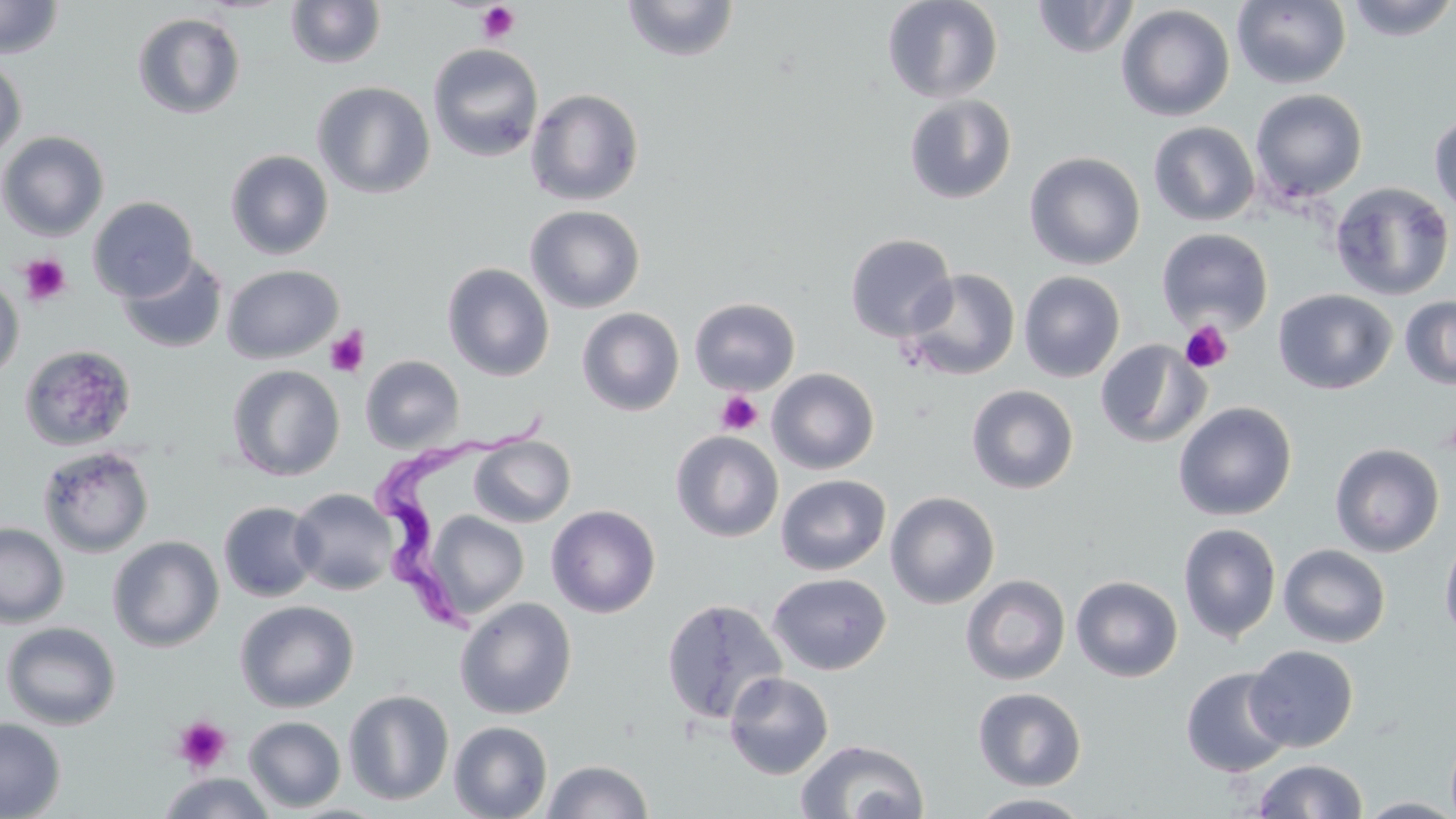 Approximate bounding boxes as (x1,y1)-(x2,y2) corner pairs in pixels. Trypanosoma brucei locations: (367,412)-(550,641). Uninfected red blood cell locations: (0,0)-(64,59), (620,0)-(740,62), (882,0)-(1003,103), (1031,0)-(1139,59), (1231,0)-(1352,89), (1343,0)-(1456,41), (285,1)-(387,69), (1116,4)-(1235,122), (131,12)-(246,120), (427,43)-(544,163), (0,57)-(27,161), (312,81)-(435,199), (526,88)-(645,206), (1249,89)-(1368,203), (904,95)-(1017,204), (1429,111)-(1456,220), (1148,121)-(1260,227), (0,130)-(109,241), (225,149)-(334,260), (1024,151)-(1146,270), (1330,181)-(1454,301), (88,196)-(199,302), (525,205)-(645,313), (1156,229)-(1274,334), (845,233)-(957,342), (116,252)-(228,354), (441,262)-(555,381), (222,264)-(343,364), (902,268)-(1021,381), (1018,271)-(1125,382), (0,274)-(24,381), (1273,288)-(1397,395), (1399,296)-(1456,389), (689,297)-(800,395), (576,307)-(685,416), (1095,340)-(1211,448), (19,344)-(137,452), (360,355)-(464,453), (227,364)-(345,481), (767,368)-(880,474), (967,385)-(1079,494), (1173,401)-(1297,520), (670,431)-(784,542), (469,435)-(575,527), (1330,442)-(1445,557), (38,445)-(155,558), (776,474)-(891,575), (290,488)-(398,595), (885,491)-(1000,609), (218,501)-(320,602), (546,504)-(660,617), (423,510)-(529,620), (0,522)-(69,628), (1178,522)-(1281,644), (1439,531)-(1456,647), (108,535)-(224,652), (1278,544)-(1391,648), (768,572)-(891,675), (960,575)-(1071,686), (1070,575)-(1183,682), (454,597)-(577,719), (660,598)-(787,725), (235,600)-(359,712), (1,622)-(121,730), (1245,644)-(1359,752), (1180,667)-(1295,778), (724,672)-(834,779), (973,687)-(1086,791), (343,689)-(454,806), (243,716)-(346,812), (0,718)-(66,819), (449,721)-(553,819), (795,738)-(929,819), (540,759)-(654,819), (1251,759)-(1369,818), (159,772)-(276,819), (967,792)-(1094,818), (1356,797)-(1456,818). Platelet locations: (476,2)-(522,45), (19,253)-(72,307), (1180,321)-(1234,373), (326,327)-(369,377), (715,390)-(763,436), (1439,418)-(1456,460), (171,716)-(232,774). Slide-level diagnosis: Trypanosoma brucei. Captured at 1000x magnification. Thin blood smear. One field of a larger specimen. Optical microscopy. May-Grünwald-Giemsa stain. Image is 1456×819 pixels.